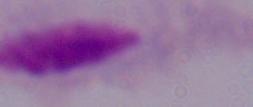
A trichomonad is seen. Micrograph. 1000x magnification.